Comment on the morphology of the red blood cells.
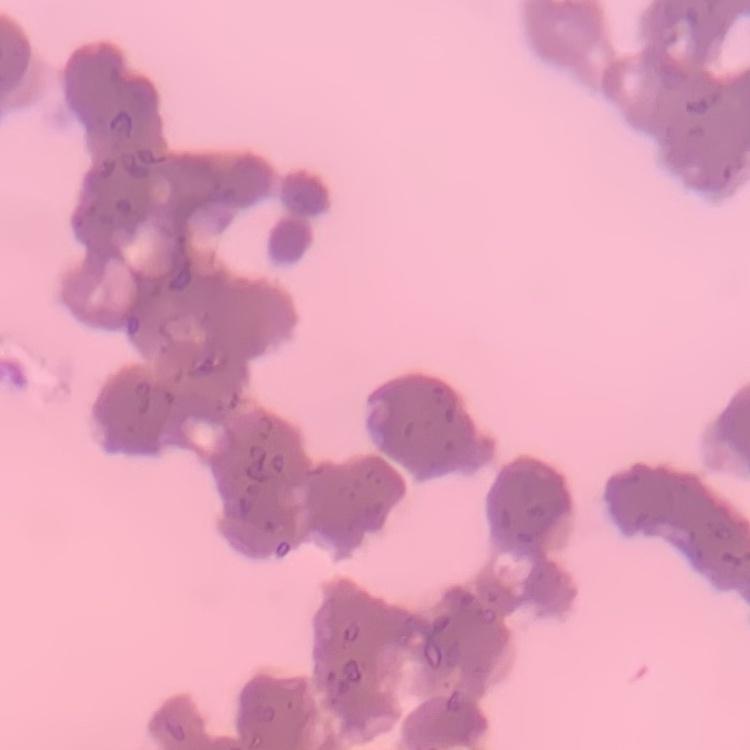
Rouleaux formation.

preparation = thin blood film
image type = square crop of a larger photomicrograph
stain = Field's or Giemsa